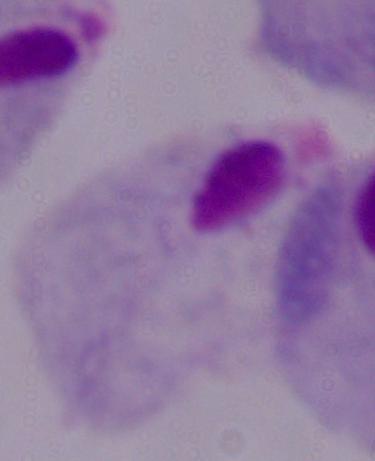
A trichomonad is seen. Micrograph. 1000x magnification.